Identify the cell.
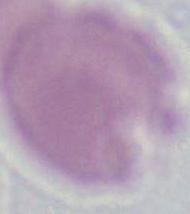
This is an erythrocyte.

{
  "modality": "micrograph",
  "magnification": "1000x"
}